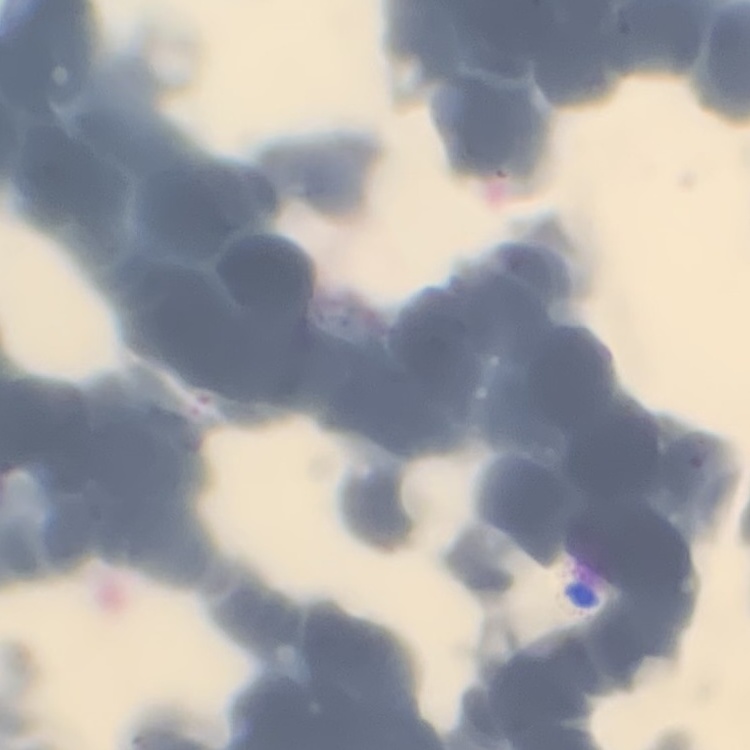

Summary:
  - Red blood cell morphology: rouleaux formation
  - Preparation: thin peripheral smear
  - Stain: Field's or Giemsa
  - Image type: one tile cut from a larger photomicrograph